Assess this cell for malaria.
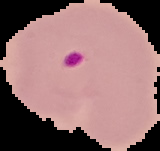
It is parasitized.

image size = 160×151 pixels
image type = cell region segmented out of the field of view; surrounding area masked to black
preparation = thin blood smear